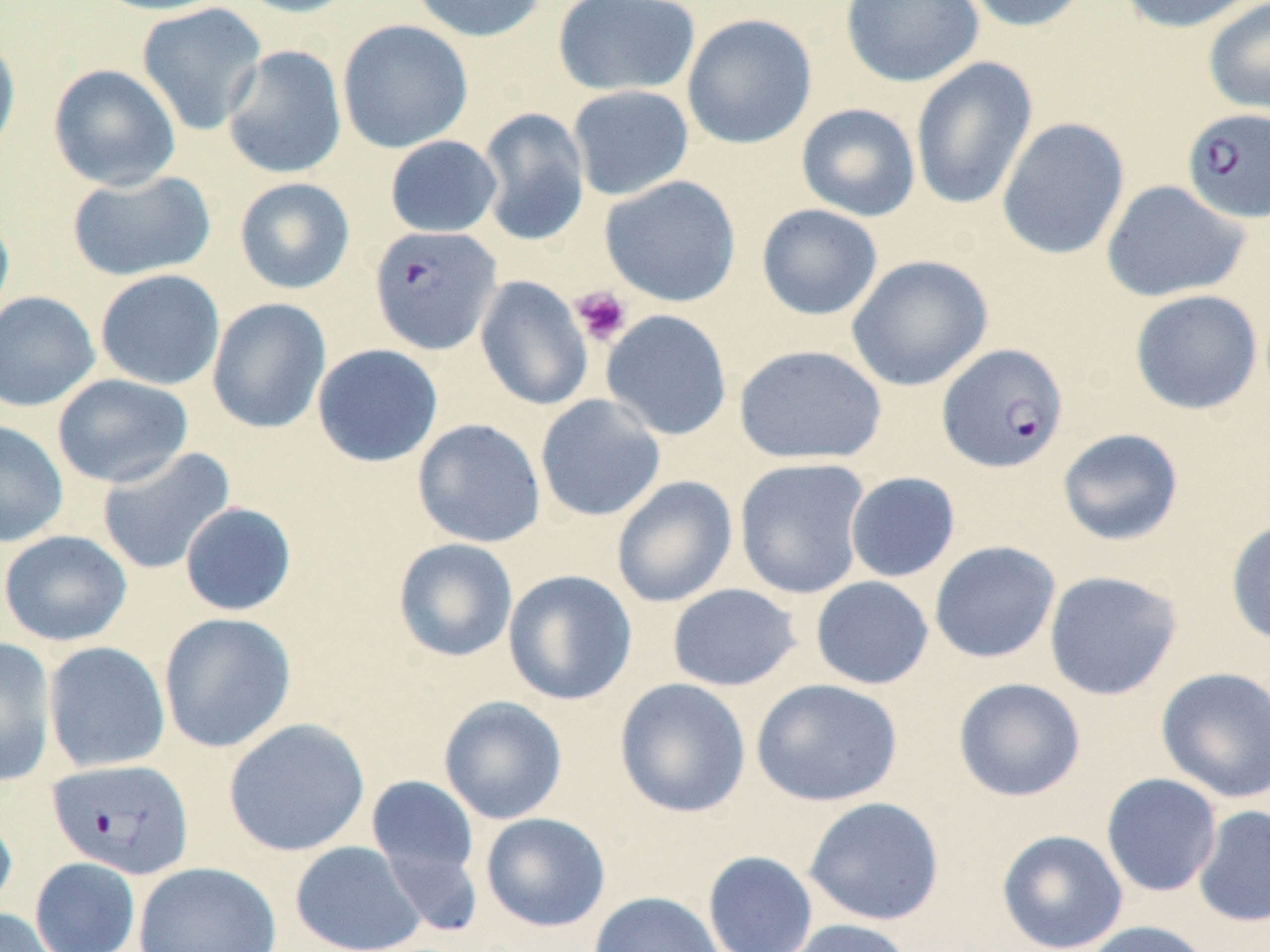

slide-level diagnosis = Plasmodium falciparum
field of view = single
stain = May-Grünwald-Giemsa
preparation = thin blood smear
uninfected red blood cell locations = approximate bounding boxes as [x1, y1, x2, y2] in pixels: [90, 0, 233, 16], [232, 0, 365, 18], [408, 0, 548, 43], [553, 0, 701, 97], [840, 0, 983, 87], [957, 0, 1094, 33], [1115, 0, 1262, 34], [136, 2, 267, 136], [1203, 2, 1270, 115], [681, 13, 817, 150], [337, 19, 473, 153], [0, 36, 21, 173], [221, 45, 347, 180], [910, 57, 1038, 212], [48, 63, 181, 191], [567, 85, 694, 201], [796, 103, 921, 221], [476, 107, 590, 247], [996, 117, 1130, 260], [384, 135, 502, 238], [66, 170, 216, 281], [600, 175, 741, 307], [234, 177, 355, 294], [1101, 179, 1250, 303], [756, 204, 883, 321], [0, 210, 15, 334], [846, 254, 993, 391], [94, 269, 226, 391], [475, 275, 593, 411], [1129, 289, 1263, 415], [0, 291, 100, 412], [207, 297, 332, 434], [601, 309, 733, 441], [312, 344, 443, 467], [733, 344, 887, 465], [51, 374, 194, 488], [535, 394, 666, 522], [412, 418, 546, 548], [0, 420, 69, 548], [1057, 428, 1184, 547], [96, 446, 235, 575], [734, 458, 871, 599], [845, 471, 961, 582], [611, 475, 738, 608], [179, 501, 297, 616], [1225, 517, 1270, 646], [0, 530, 133, 647], [392, 538, 519, 663], [929, 540, 1061, 663], [503, 569, 637, 706], [1043, 570, 1182, 701], [810, 576, 934, 690], [667, 583, 802, 692], [158, 612, 297, 753], [0, 637, 57, 787], [43, 641, 170, 773], [1155, 666, 1270, 804], [614, 677, 752, 818], [953, 677, 1086, 802], [751, 678, 903, 807], [438, 695, 568, 824], [222, 717, 371, 857], [364, 773, 483, 921], [1100, 773, 1223, 898], [803, 796, 945, 926], [1192, 805, 1270, 927], [0, 807, 18, 917], [480, 812, 611, 932], [996, 829, 1128, 952], [290, 841, 426, 952], [703, 850, 819, 952], [30, 857, 140, 952], [133, 861, 281, 952], [588, 891, 726, 952], [0, 907, 60, 952], [777, 918, 918, 952], [1081, 920, 1214, 952]
Plasmodium falciparum-infected red blood cell locations = approximate bounding boxes as [x1, y1, x2, y2] in pixels: [1181, 107, 1270, 223], [369, 225, 502, 355], [937, 343, 1069, 473], [47, 758, 195, 880]
platelet locations = approximate bounding boxes as [x1, y1, x2, y2] in pixels: [570, 286, 633, 346]
magnification = 1000x
modality = light microscopy
image size = 1270×952 pixels